Name the parasite shown.
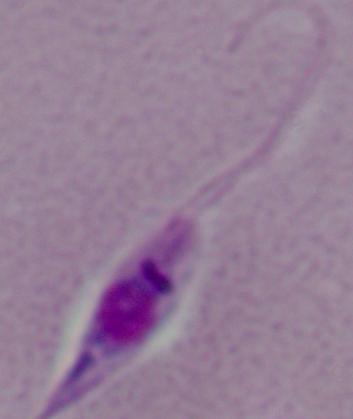
Leishmania.

Micrograph. Captured at 1000x magnification.